Comment on the morphology of the erythrocytes.
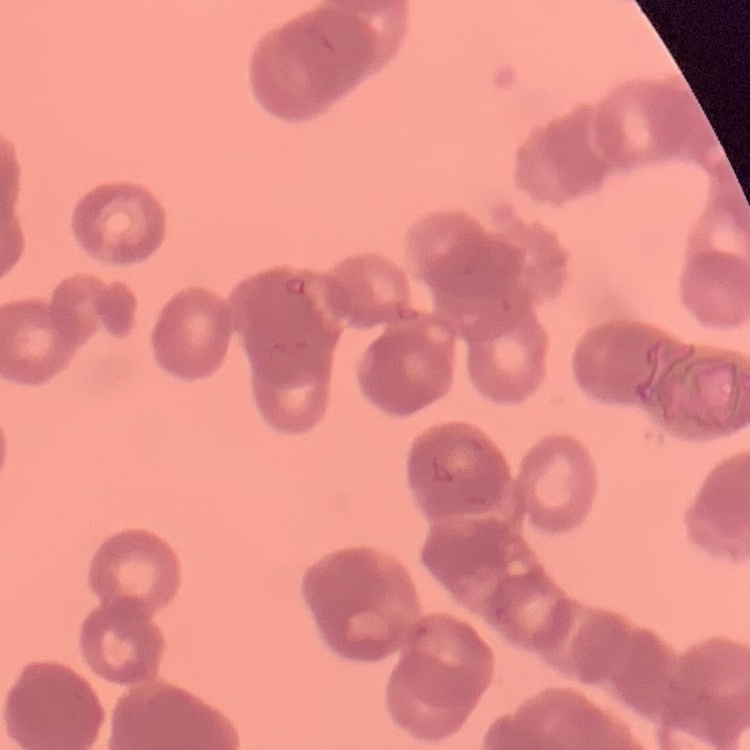
They show rouleaux formation.

Summary:
  - Stain: Field's or Giemsa
  - Image type: square crop of a larger photomicrograph
  - Preparation: thin blood smear